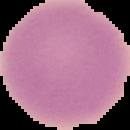
image_type: cell region segmented out of the field of view; surrounding area masked to black
image_size: 130×130 pixels
preparation: thin blood film
malaria_status: uninfected